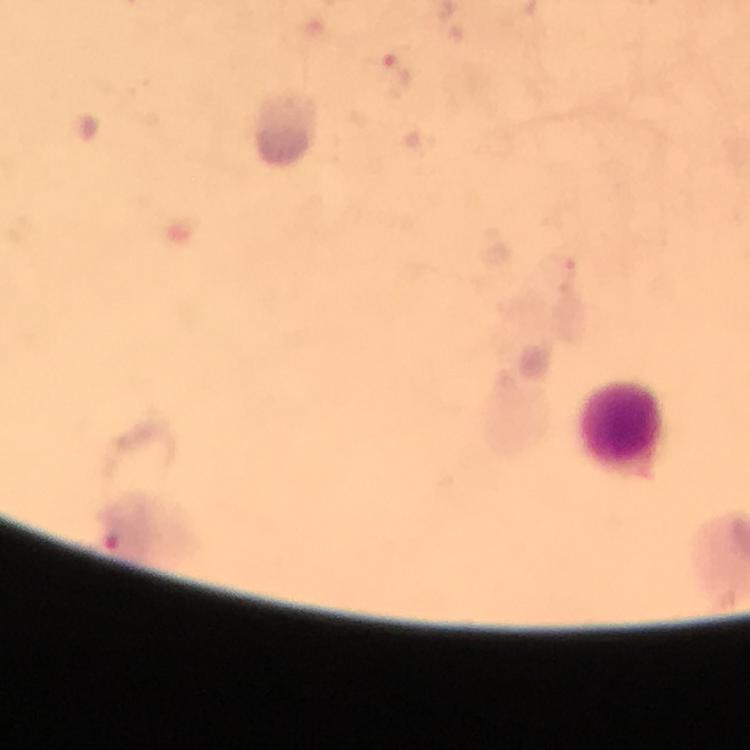 Approximate centers as [x, y] in pixels. Leukocyte locations: [625, 428]. Malaria parasite locations: [394, 77]. Giemsa-stained preparation. Image is 750×750 pixels. At 100x magnification. From a malaria diagnostic workup. Thick blood smear. A crop from one field of view. Photographed with a smartphone mounted on the microscope. Immersion oil applied.